Report the malaria status of this cell.
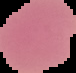
Uninfected.

{
  "image_type": "cell region segmented out of the field of view; surrounding area masked to black",
  "image_size": "76×73 pixels",
  "preparation": "thin blood film"
}